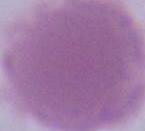
Summary:
  - Modality: photomicrograph
  - Identification: erythrocyte
  - Magnification: 1000x